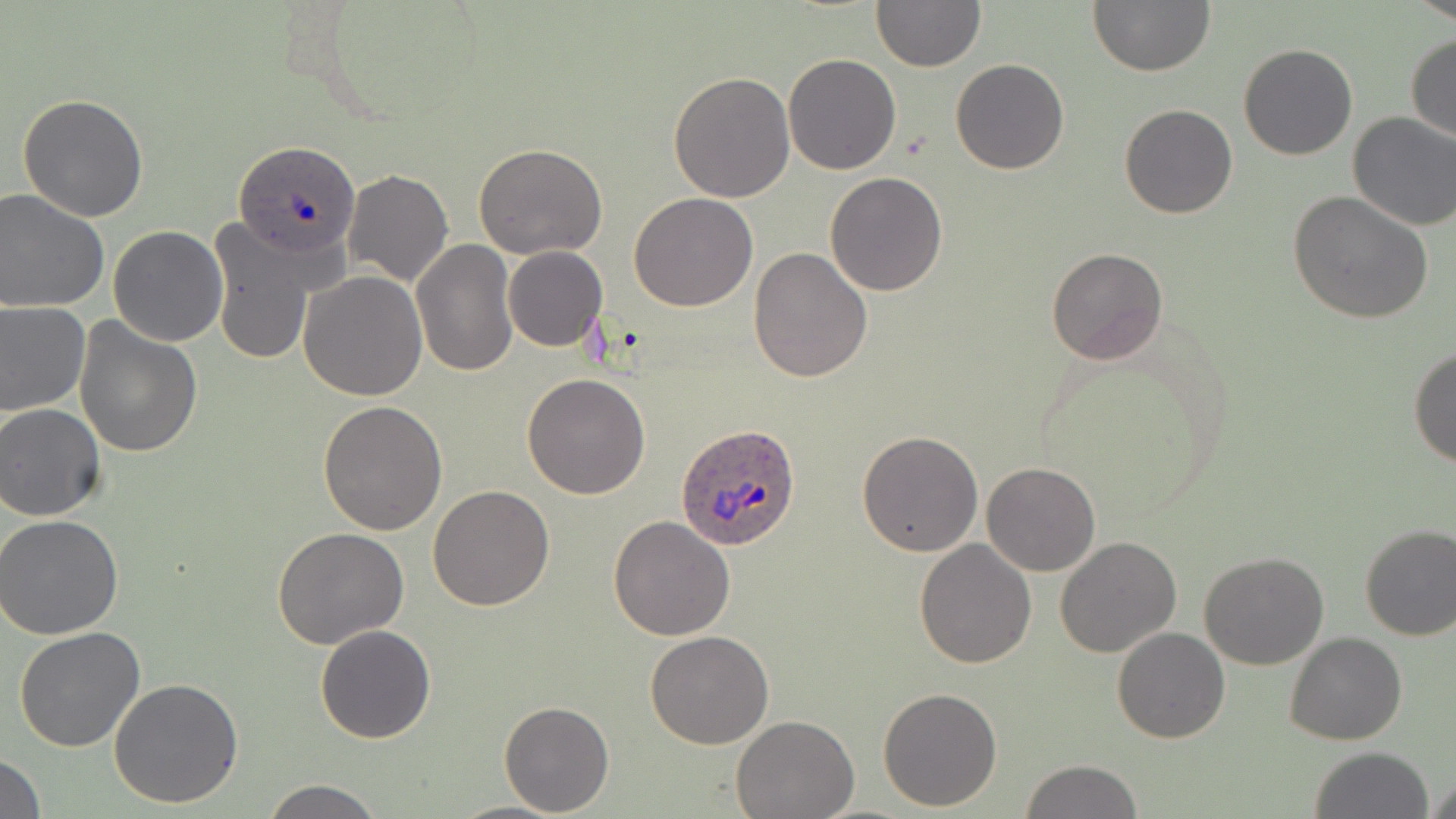
Summary:
  - Coordinate format: approximate bounding boxes as named x1/y1/x2/y2 corners in pixels
  - Uninfected red blood cell locations: (x1=870, y1=0, x2=984, y2=71), (x1=1413, y1=0, x2=1456, y2=25), (x1=1088, y1=1, x2=1214, y2=76), (x1=1405, y1=34, x2=1456, y2=145), (x1=1238, y1=43, x2=1358, y2=161), (x1=784, y1=53, x2=901, y2=174), (x1=951, y1=57, x2=1070, y2=175), (x1=668, y1=71, x2=795, y2=202), (x1=17, y1=94, x2=150, y2=222), (x1=1119, y1=103, x2=1237, y2=218), (x1=1347, y1=111, x2=1456, y2=232), (x1=473, y1=144, x2=608, y2=261), (x1=342, y1=169, x2=453, y2=288), (x1=825, y1=172, x2=947, y2=295), (x1=0, y1=189, x2=111, y2=312), (x1=1289, y1=190, x2=1434, y2=324), (x1=629, y1=192, x2=759, y2=312), (x1=206, y1=219, x2=327, y2=366), (x1=108, y1=226, x2=228, y2=347), (x1=411, y1=241, x2=519, y2=378), (x1=748, y1=246, x2=873, y2=382), (x1=1046, y1=246, x2=1169, y2=366), (x1=502, y1=247, x2=608, y2=352), (x1=298, y1=270, x2=427, y2=401), (x1=0, y1=300, x2=92, y2=416), (x1=73, y1=316, x2=202, y2=457), (x1=1409, y1=348, x2=1456, y2=468), (x1=522, y1=373, x2=651, y2=499), (x1=319, y1=400, x2=449, y2=536), (x1=0, y1=402, x2=107, y2=522), (x1=857, y1=430, x2=984, y2=556), (x1=982, y1=462, x2=1100, y2=576), (x1=428, y1=484, x2=555, y2=611), (x1=0, y1=516, x2=126, y2=638), (x1=608, y1=516, x2=735, y2=641), (x1=1358, y1=523, x2=1456, y2=641), (x1=274, y1=525, x2=408, y2=649), (x1=1055, y1=537, x2=1182, y2=657), (x1=915, y1=539, x2=1037, y2=668), (x1=1198, y1=552, x2=1330, y2=670), (x1=315, y1=625, x2=436, y2=743), (x1=15, y1=627, x2=146, y2=751), (x1=1113, y1=628, x2=1229, y2=744), (x1=646, y1=631, x2=773, y2=749), (x1=1284, y1=633, x2=1406, y2=745), (x1=108, y1=677, x2=245, y2=810), (x1=877, y1=687, x2=1003, y2=812), (x1=499, y1=700, x2=614, y2=816), (x1=730, y1=715, x2=858, y2=819), (x1=1308, y1=747, x2=1434, y2=819), (x1=0, y1=752, x2=46, y2=818), (x1=1020, y1=759, x2=1143, y2=818), (x1=1425, y1=774, x2=1456, y2=819), (x1=260, y1=777, x2=385, y2=818), (x1=446, y1=801, x2=567, y2=818)
  - Plasmodium ovale-infected red blood cell locations: (x1=235, y1=144, x2=364, y2=262), (x1=676, y1=425, x2=803, y2=550)
  - Slide-level diagnosis: Plasmodium ovale
  - Magnification: 1000x
  - Modality: light microscopy
  - Stain: May-Grünwald-Giemsa
  - Preparation: thin blood film
  - Image size: 1456×819 pixels
  - Field of view: single